Report the malaria status of this cell.
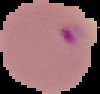
Parasitized.

image size = 100×94 pixels
preparation = thin blood film
image type = segmented cell region with the area outside set to black